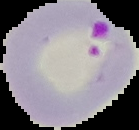
{
  "image_type": "segmented cell region with the area outside set to black",
  "result": "malaria parasites identified",
  "image_size": "139×130 pixels",
  "preparation": "thin blood film"
}